Classify this cell by malaria status.
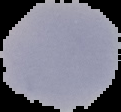

Uninfected.

Segmented cell region on a black background. Image is 121×112 pixels. From a thin blood smear.